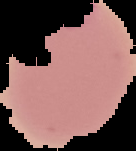 The area outside the segmented cell region is set to black. Image is 136×151 pixels. Result: malaria parasites identified. From a thin blood film.